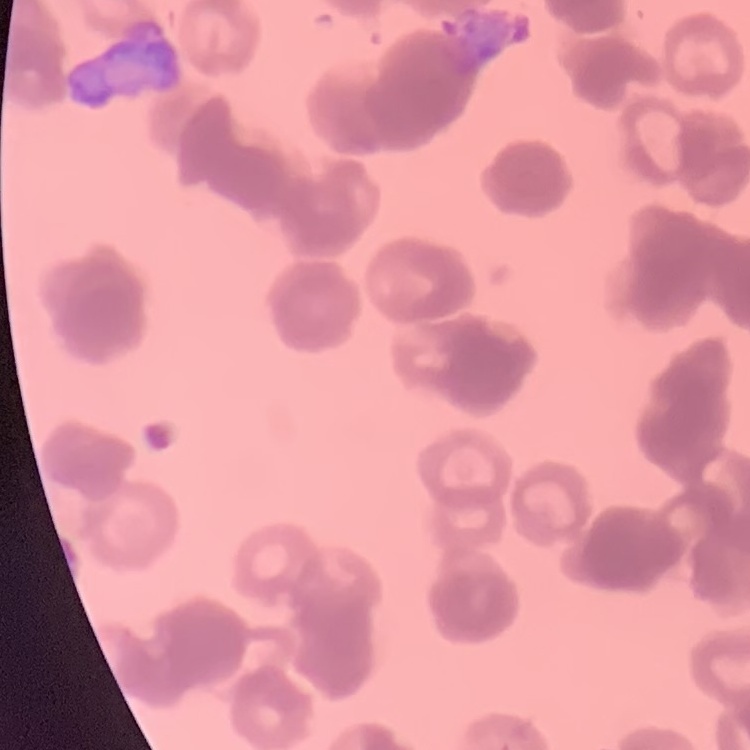
red blood cell morphology = rouleaux formation
stain = Field's or Giemsa
preparation = thin blood film
image type = square crop of a larger photomicrograph